Describe the morphology of the erythrocytes.
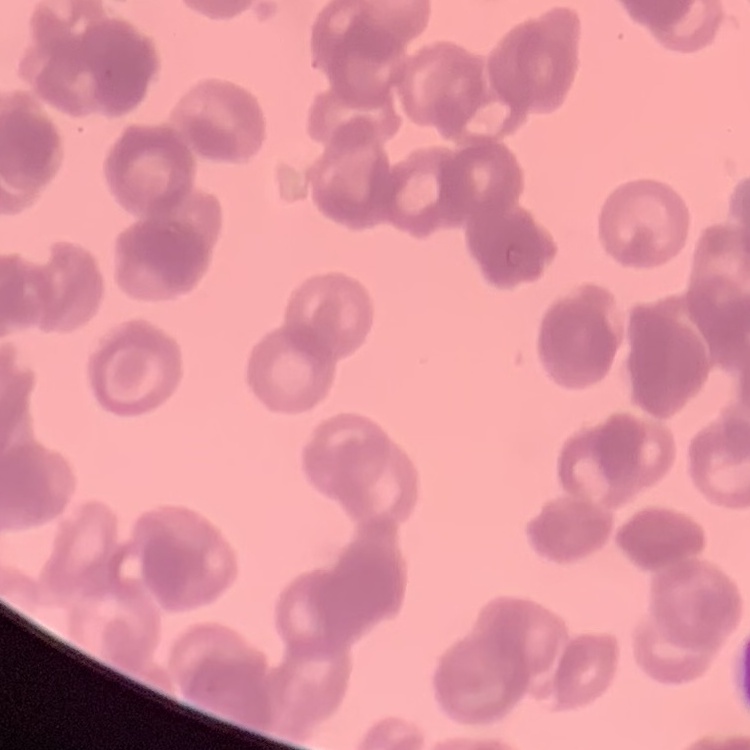

They show rouleaux formation.

stain = Field's or Giemsa
image type = one tile cut from a larger photomicrograph
preparation = thin blood film